Identify the blood parasite species.
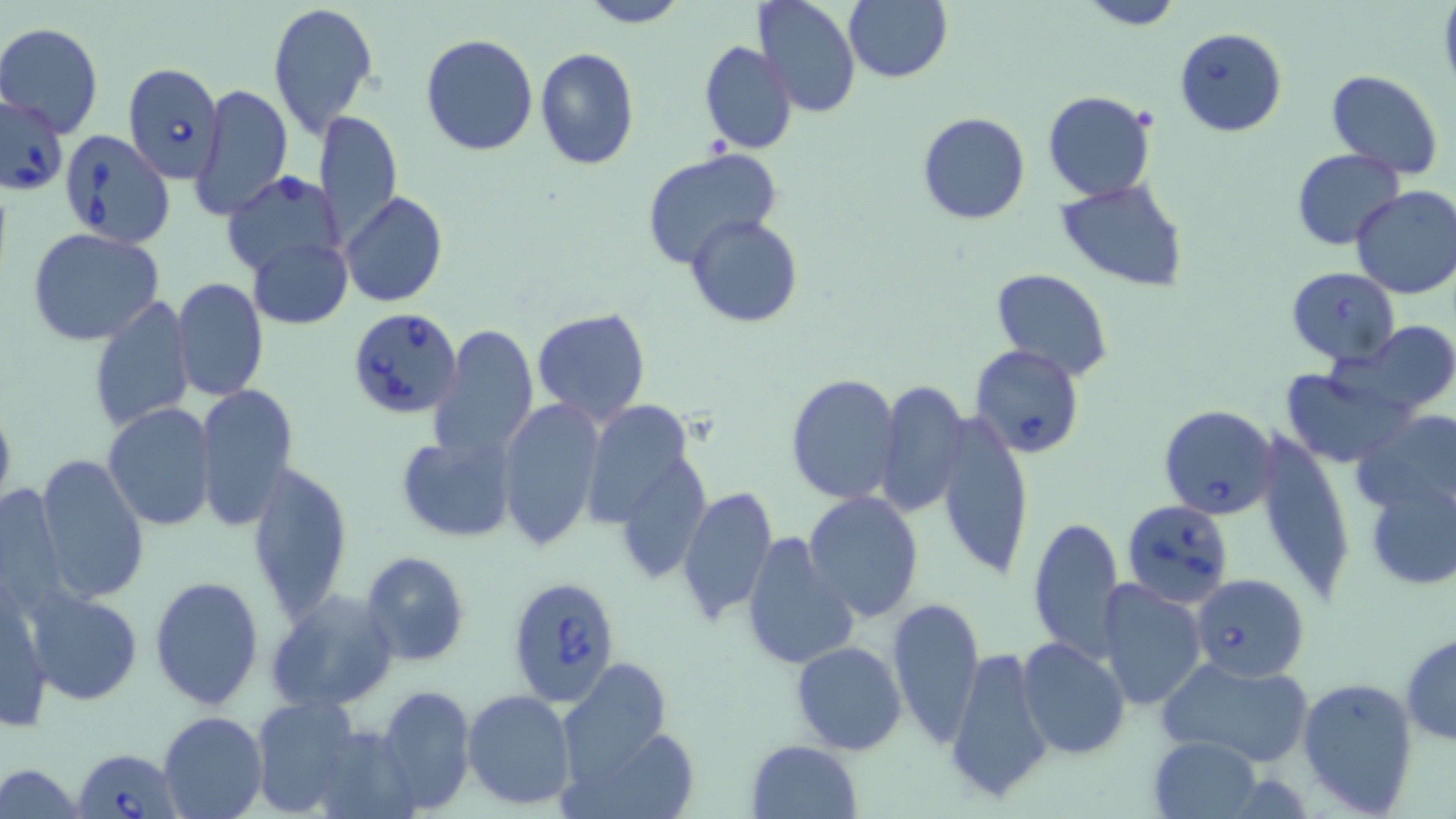

Babesia divergens.

Approximate bounding boxes as (x1, y1, x2, y2) in pixels. Uninfected red blood cell locations: (578, 0, 690, 27), (754, 0, 861, 119), (844, 0, 951, 83), (1077, 0, 1182, 29), (266, 1, 379, 139), (1, 24, 102, 133), (421, 34, 539, 155), (699, 40, 797, 155), (535, 47, 640, 169), (1326, 70, 1443, 178), (192, 83, 294, 221), (1043, 91, 1156, 201), (315, 109, 404, 240), (917, 112, 1032, 225), (642, 148, 783, 267), (1291, 148, 1405, 251), (222, 172, 347, 283), (1054, 178, 1188, 291), (1351, 185, 1456, 299), (340, 192, 448, 308), (686, 213, 805, 327), (27, 228, 166, 347), (249, 236, 353, 328), (990, 268, 1112, 383), (171, 278, 269, 401), (88, 294, 194, 434), (531, 308, 652, 425), (1345, 322, 1456, 418), (429, 323, 537, 465), (1279, 365, 1410, 468), (786, 373, 901, 504), (876, 381, 969, 517), (194, 383, 299, 529), (499, 397, 605, 552), (589, 399, 688, 529), (0, 401, 17, 520), (103, 404, 217, 532), (1350, 409, 1456, 520), (935, 412, 1034, 584), (1251, 429, 1354, 603), (397, 436, 518, 542), (35, 453, 151, 604), (629, 459, 712, 584), (248, 460, 353, 624), (1364, 478, 1454, 589), (1, 481, 70, 611), (675, 484, 778, 628), (804, 491, 924, 624), (1028, 514, 1125, 661), (740, 531, 858, 669), (359, 551, 470, 667), (149, 576, 264, 709), (1098, 581, 1207, 712), (1, 584, 53, 734), (266, 589, 397, 713), (26, 590, 143, 705), (885, 598, 986, 745), (1401, 633, 1456, 745), (1015, 637, 1131, 760), (790, 641, 907, 754), (944, 646, 1054, 807), (1157, 655, 1316, 767), (558, 659, 672, 782), (1296, 675, 1420, 814), (376, 684, 476, 812), (462, 688, 575, 809), (250, 697, 364, 816), (158, 711, 268, 819), (566, 720, 699, 819), (306, 725, 416, 818), (1149, 736, 1263, 819), (746, 739, 862, 819), (0, 761, 86, 817). Babesia divergens-infected red blood cell locations: (1174, 28, 1287, 137), (123, 62, 225, 183), (1, 96, 69, 195), (65, 132, 173, 248), (1285, 267, 1399, 366), (347, 307, 463, 421), (969, 344, 1085, 458), (1160, 403, 1278, 520), (1122, 499, 1233, 608), (1189, 573, 1310, 681), (507, 574, 622, 707), (72, 748, 181, 819). May-Grünwald-Giemsa-stained preparation. Thin blood smear. Image is 1456×819 pixels. Light microscopy. 1000x magnification. One field of a larger specimen.